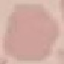
result = negative for malaria parasites
preparation = thin smear
capture = smartphone through the microscope eyepiece
image type = cell patch, automatically extracted from a larger field of view and resized to 64 × 64 pixels
stain = Giemsa